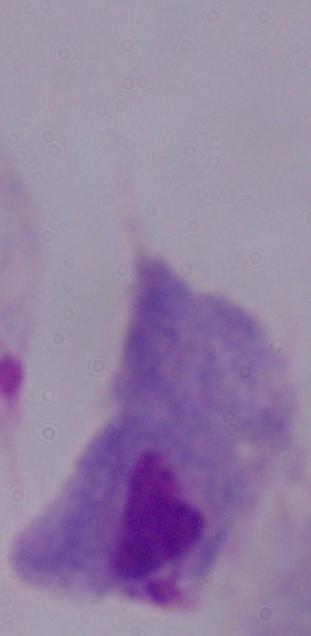
modality = micrograph
magnification = 1000x
identification = trichomonad